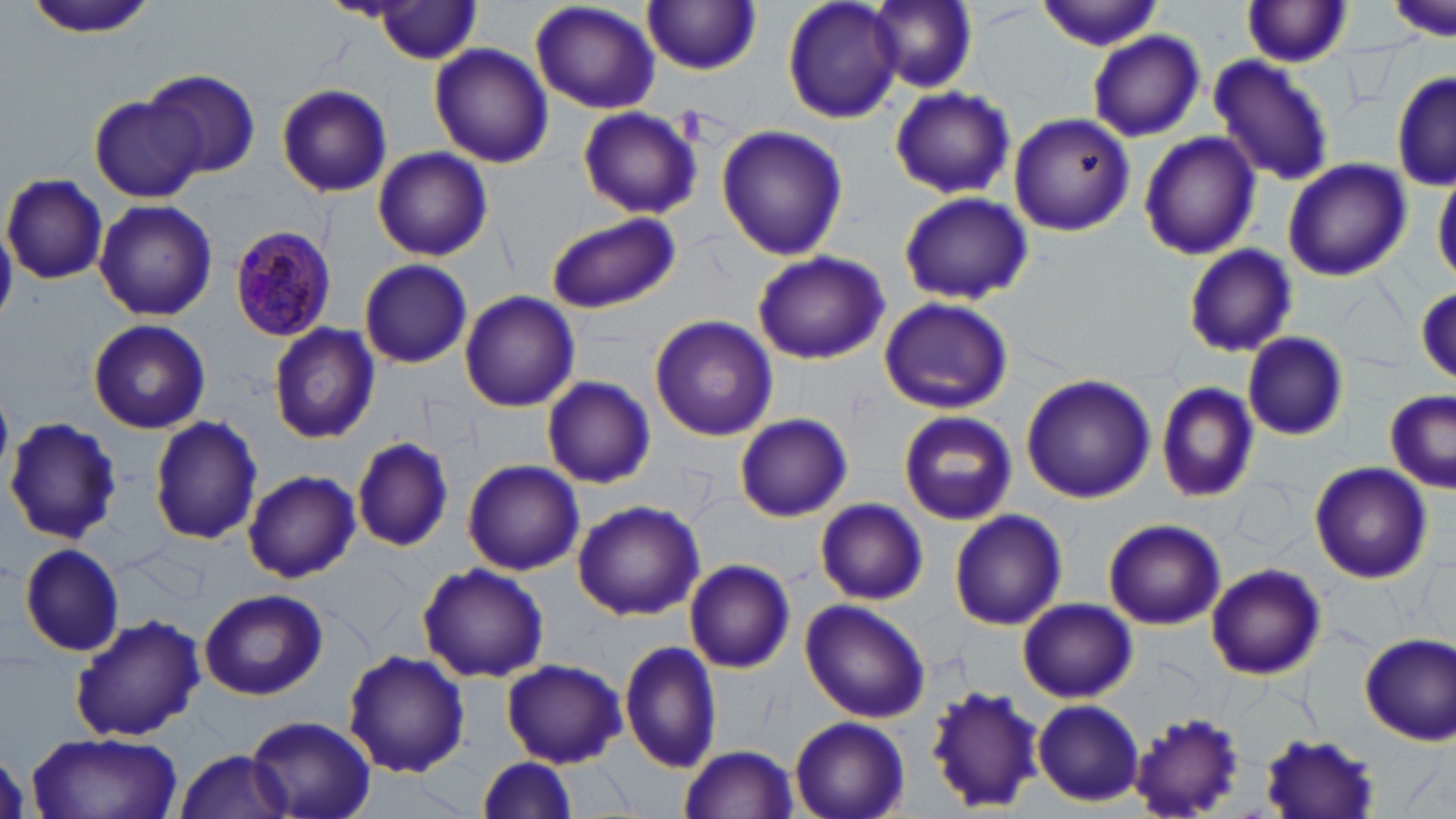
Approximate bounding boxes as (x1,y1)-(x2,y2) corner pairs in pixels. Plasmodium malariae-infected red blood cell locations: (231,225)-(336,341). Uninfected red blood cell locations: (528,0)-(661,114), (782,0)-(905,123), (869,0)-(977,92), (1385,0)-(1456,42), (21,1)-(158,41), (1037,1)-(1166,51), (364,2)-(486,63), (643,2)-(763,74), (1241,2)-(1354,69), (1086,30)-(1205,142), (429,43)-(553,169), (1208,54)-(1334,185), (145,68)-(261,178), (1392,69)-(1455,192), (276,84)-(392,198), (889,86)-(1015,200), (89,96)-(205,202), (577,105)-(703,220), (1008,114)-(1134,238), (716,125)-(847,262), (1138,132)-(1261,261), (373,146)-(492,261), (1281,159)-(1412,283), (1433,168)-(1456,288), (4,174)-(107,282), (899,191)-(1032,306), (92,199)-(218,321), (544,212)-(680,314), (1181,244)-(1297,359), (751,250)-(890,366), (358,259)-(472,368), (1414,287)-(1455,384), (460,291)-(578,412), (878,297)-(1014,415), (650,316)-(777,442), (88,319)-(211,434), (267,321)-(380,443), (1240,332)-(1348,440), (1181,349)-(1291,467), (1019,373)-(1157,504), (542,376)-(656,488), (1154,380)-(1260,504), (1382,389)-(1456,490), (898,411)-(1017,526), (735,413)-(853,521), (149,415)-(264,545), (4,416)-(121,546), (352,436)-(454,551), (461,461)-(584,575), (1311,462)-(1433,583), (242,470)-(360,583), (815,498)-(928,604), (571,499)-(705,621), (950,508)-(1067,631), (1104,519)-(1226,630), (17,543)-(126,656), (685,558)-(796,673), (416,562)-(549,683), (1206,563)-(1326,681), (198,588)-(328,700), (799,597)-(930,722), (1018,598)-(1136,703), (70,612)-(206,742), (1360,635)-(1455,745), (619,637)-(722,774), (342,650)-(470,776), (500,659)-(627,766), (924,683)-(1047,813), (1033,699)-(1144,805), (1126,709)-(1248,819), (247,712)-(377,819), (788,715)-(909,819), (1256,727)-(1381,819), (25,731)-(183,819), (678,745)-(799,818), (173,749)-(292,818), (470,756)-(580,819). Slide-level diagnosis: Plasmodium malariae. Thin blood smear. May-Grünwald-Giemsa-stained preparation. Light microscopy. Image is 1456×819 pixels. Single field of view. Captured at 1000x magnification.